Outline each blood parasite and name the species.
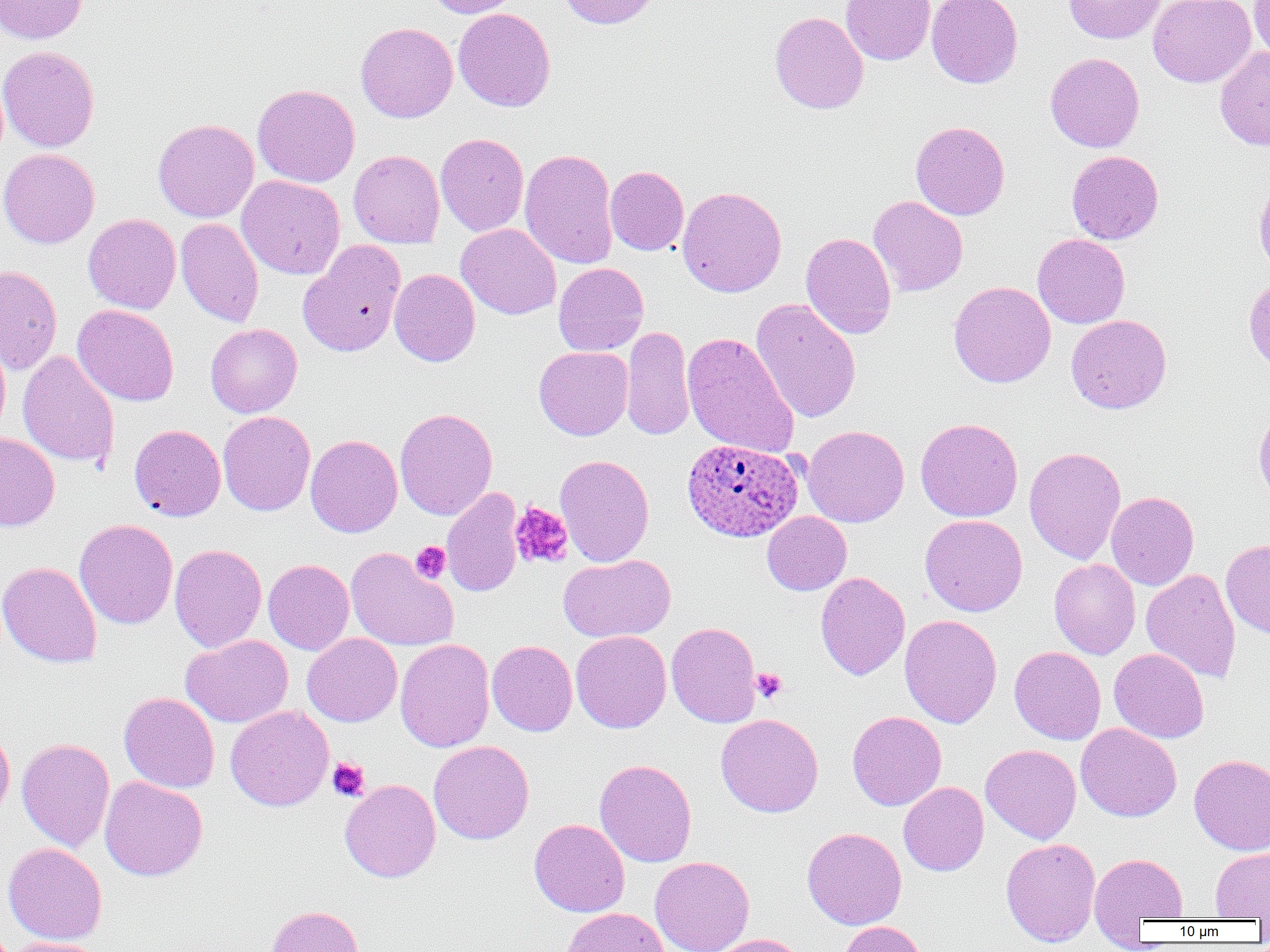
Approximate bounding boxes as [x1, y1, x2, y2] in pixels.
Plasmodium ovale-infected red blood cells: [682, 439, 804, 542].
No Plasmodium falciparum, Plasmodium malariae, Plasmodium vivax, Babesia divergens, or Trypanosoma brucei observed.

Uninfected red blood cell locations: [0, 0, 89, 44], [424, 0, 521, 18], [558, 0, 662, 29], [841, 0, 935, 65], [926, 0, 1023, 89], [1063, 0, 1166, 44], [1148, 0, 1256, 88], [1250, 0, 1270, 64], [453, 8, 556, 112], [769, 11, 868, 114], [355, 22, 458, 123], [0, 45, 100, 152], [1215, 46, 1270, 151], [1045, 52, 1145, 152], [252, 84, 360, 187], [153, 118, 259, 222], [910, 121, 1010, 220], [435, 133, 529, 236], [0, 148, 100, 249], [519, 148, 618, 270], [348, 150, 444, 248], [1066, 150, 1163, 244], [605, 165, 689, 255], [236, 175, 345, 280], [1253, 176, 1270, 279], [677, 186, 787, 297], [868, 195, 968, 296], [83, 213, 181, 314], [176, 218, 264, 328], [456, 223, 561, 320], [801, 232, 896, 339], [1032, 233, 1130, 328], [299, 241, 407, 357], [553, 263, 648, 356], [0, 265, 62, 375], [389, 269, 480, 367], [948, 281, 1056, 388], [750, 298, 861, 423], [72, 304, 179, 406], [1066, 315, 1171, 414], [205, 323, 302, 418], [621, 325, 695, 441], [682, 332, 799, 458], [0, 333, 11, 439], [534, 346, 633, 440], [17, 349, 120, 469], [1254, 407, 1270, 507], [395, 408, 497, 520], [218, 411, 315, 516], [915, 417, 1023, 522], [129, 424, 226, 521], [802, 425, 909, 527], [0, 433, 60, 531], [305, 434, 402, 537], [1024, 446, 1126, 564], [555, 454, 654, 567], [442, 487, 524, 597], [1106, 491, 1199, 591], [762, 512, 851, 595], [920, 514, 1027, 616], [74, 518, 178, 629], [1221, 538, 1270, 637], [169, 543, 267, 653], [345, 547, 459, 652], [559, 554, 675, 643], [1049, 558, 1140, 659], [263, 559, 354, 655], [0, 561, 102, 668], [1140, 568, 1241, 683], [815, 572, 910, 680], [899, 615, 1002, 728], [666, 622, 760, 728], [571, 630, 671, 733], [302, 633, 402, 727], [181, 635, 293, 728], [395, 638, 494, 753], [487, 640, 578, 736], [1009, 647, 1106, 744], [1109, 648, 1209, 743], [119, 692, 220, 793], [226, 705, 334, 812], [847, 711, 946, 810], [716, 713, 823, 817], [1076, 723, 1181, 822], [0, 724, 15, 824], [17, 738, 114, 851], [428, 740, 534, 845], [980, 744, 1082, 844], [1189, 754, 1270, 855], [594, 759, 697, 867], [100, 776, 208, 881], [340, 779, 441, 883], [899, 782, 988, 876], [529, 818, 630, 917], [802, 827, 907, 929], [1001, 838, 1101, 947], [3, 842, 107, 944], [1210, 848, 1270, 920], [1089, 852, 1189, 928], [649, 856, 755, 952], [264, 905, 364, 952], [560, 907, 669, 952], [838, 921, 928, 952], [709, 933, 808, 952], [5, 937, 107, 952]. Platelet locations: [509, 501, 574, 568], [411, 541, 450, 583], [751, 668, 787, 703], [327, 757, 370, 801]. Slide-level diagnosis: Plasmodium ovale. 1000x magnification. Single field of view. Thin blood film. Image is 1270×952 pixels. Light microscopy.